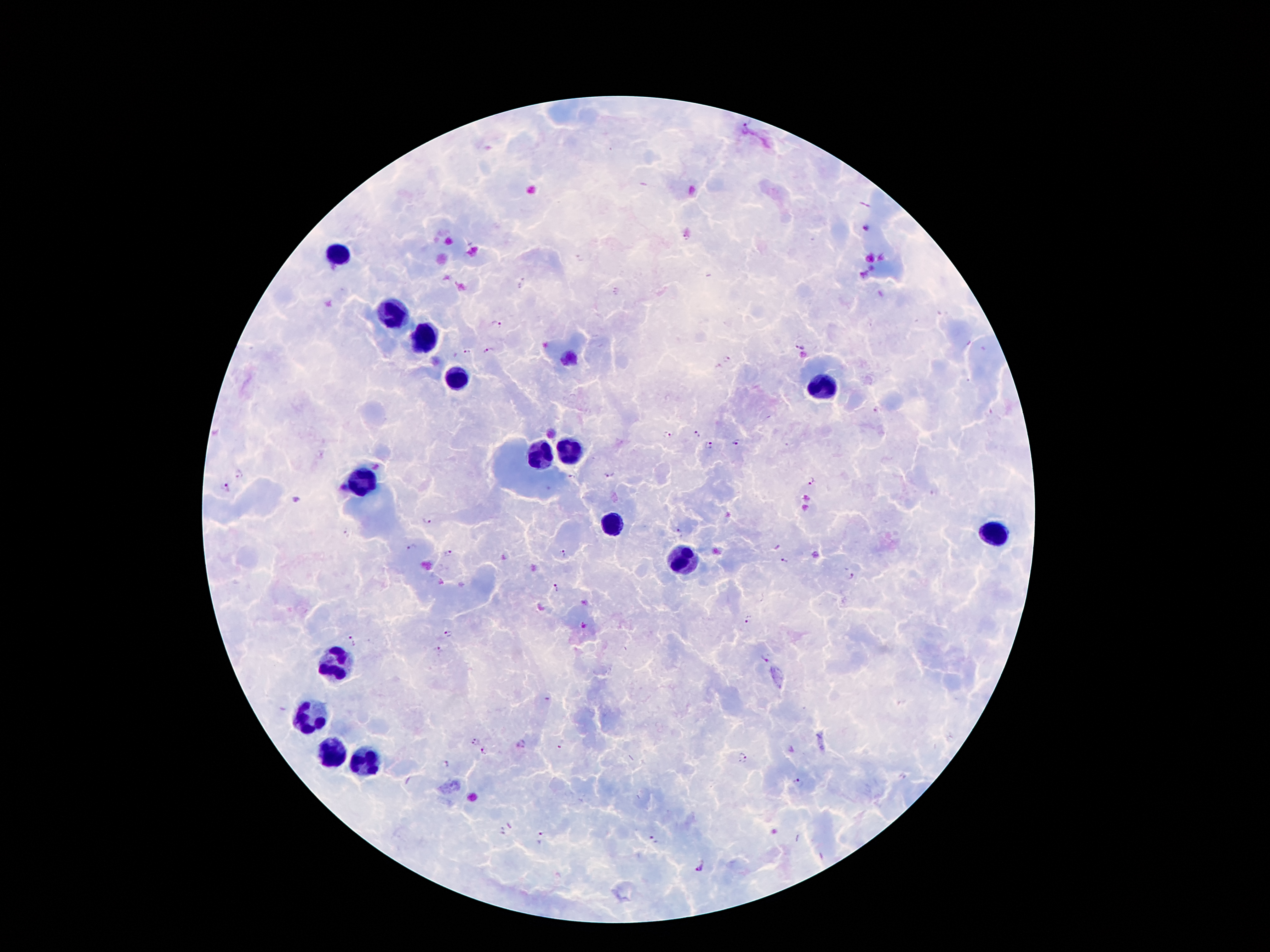

Approximate object centers, in pixels from the top-left corner. Malaria parasite locations: (x=865, y=229), (x=686, y=237), (x=616, y=291), (x=496, y=324), (x=799, y=346), (x=489, y=352), (x=468, y=354), (x=728, y=360), (x=697, y=434), (x=668, y=435), (x=709, y=445), (x=736, y=445), (x=238, y=474), (x=608, y=475), (x=572, y=477), (x=811, y=481), (x=225, y=487), (x=426, y=521), (x=348, y=532), (x=678, y=534), (x=412, y=549), (x=565, y=553), (x=449, y=554), (x=785, y=561), (x=850, y=577), (x=556, y=589), (x=748, y=618), (x=584, y=625), (x=447, y=634), (x=352, y=640), (x=440, y=651), (x=765, y=660), (x=474, y=740), (x=522, y=744), (x=484, y=751), (x=743, y=758), (x=446, y=764), (x=798, y=784), (x=509, y=825), (x=502, y=832), (x=542, y=838), (x=654, y=839), (x=702, y=868). Leukocyte locations: (x=338, y=258), (x=393, y=313), (x=426, y=342), (x=455, y=382), (x=823, y=388), (x=567, y=454), (x=537, y=458), (x=365, y=481), (x=607, y=521), (x=995, y=536), (x=680, y=563), (x=338, y=664), (x=311, y=714), (x=330, y=752), (x=367, y=767). Thick blood smear. 100x magnification. Image is 1270×952 pixels. Single field of view. Photographed through the microscope eyepiece with a smartphone camera. Giemsa-stained preparation. Patient malaria status: infected with Plasmodium falciparum.